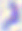

identification: Toxoplasma gondii
modality: micrograph
magnification: 400x